Locate every uninfected red blood cell.
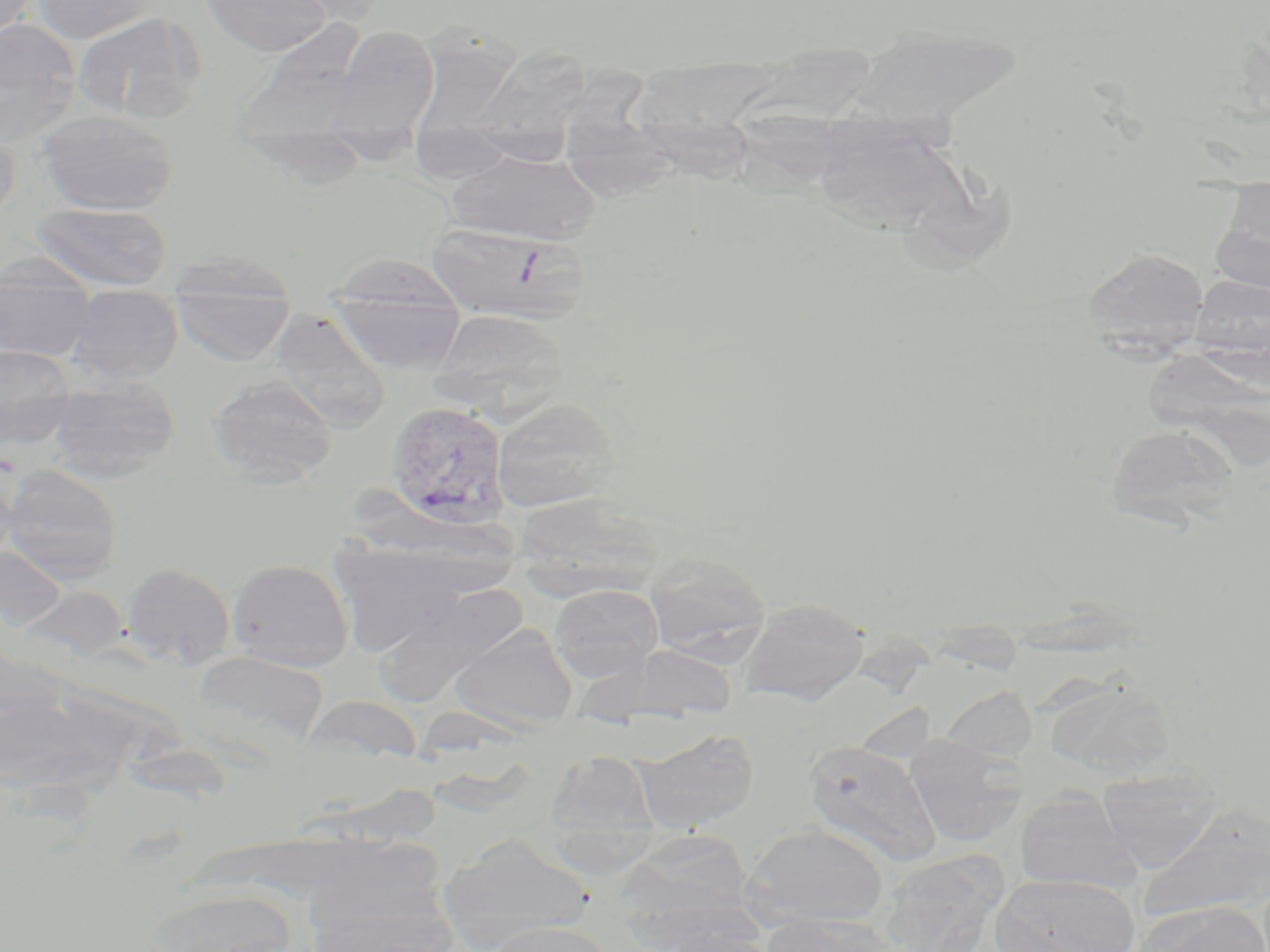
Approximate bounding boxes as (x1, y1, x2, y2) in pixels.
Uninfected red blood cells: (0, 0, 40, 40), (33, 0, 164, 43), (201, 0, 332, 57), (286, 0, 394, 26), (72, 11, 206, 124), (0, 18, 83, 145), (239, 19, 375, 144), (848, 23, 1024, 131), (328, 27, 441, 137), (410, 29, 522, 139), (472, 43, 593, 151), (641, 57, 772, 193), (564, 61, 669, 210), (37, 109, 178, 215), (815, 114, 945, 233), (412, 120, 517, 185), (0, 123, 21, 227), (448, 148, 600, 244), (1211, 199, 1270, 295), (32, 203, 173, 292), (427, 223, 587, 325), (1083, 248, 1209, 352), (169, 254, 296, 366), (0, 256, 98, 363), (327, 261, 467, 374), (1191, 276, 1270, 356), (65, 284, 183, 384), (270, 309, 392, 431), (431, 309, 569, 414), (1145, 344, 1266, 468), (0, 346, 77, 450), (209, 374, 337, 485), (47, 376, 179, 481), (492, 398, 621, 513), (1107, 424, 1238, 529), (0, 457, 20, 569), (2, 464, 123, 584), (329, 539, 470, 657), (643, 552, 772, 664), (227, 558, 353, 672), (122, 563, 236, 669), (389, 579, 529, 702), (549, 583, 664, 681), (739, 598, 870, 706), (450, 623, 578, 731), (626, 644, 739, 719), (191, 650, 329, 749), (1048, 679, 1176, 781), (940, 685, 1037, 760), (634, 730, 759, 832), (905, 736, 1027, 847), (803, 738, 941, 866), (547, 751, 659, 845), (1095, 765, 1222, 872), (1014, 791, 1141, 895), (1136, 805, 1270, 925), (742, 823, 890, 928), (624, 829, 756, 922), (438, 836, 594, 950), (878, 852, 1006, 952), (989, 873, 1138, 952), (304, 885, 460, 952), (144, 886, 297, 952), (1136, 901, 1270, 952), (763, 914, 894, 952), (486, 920, 619, 952).

Plasmodium vivax-infected red blood cell locations: (386, 400, 511, 530). Slide-level diagnosis: Plasmodium vivax. May-Grünwald-Giemsa-stained preparation. Image is 1270×952 pixels. One field of a larger specimen. 1000x magnification. Optical microscopy. Thin blood film.